Assess this cell for malaria.
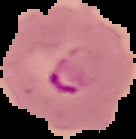
Parasitized.

From a thin blood smear. Cell region segmented out of the field of view; the surrounding area is masked to black. Image is 136×139 pixels.